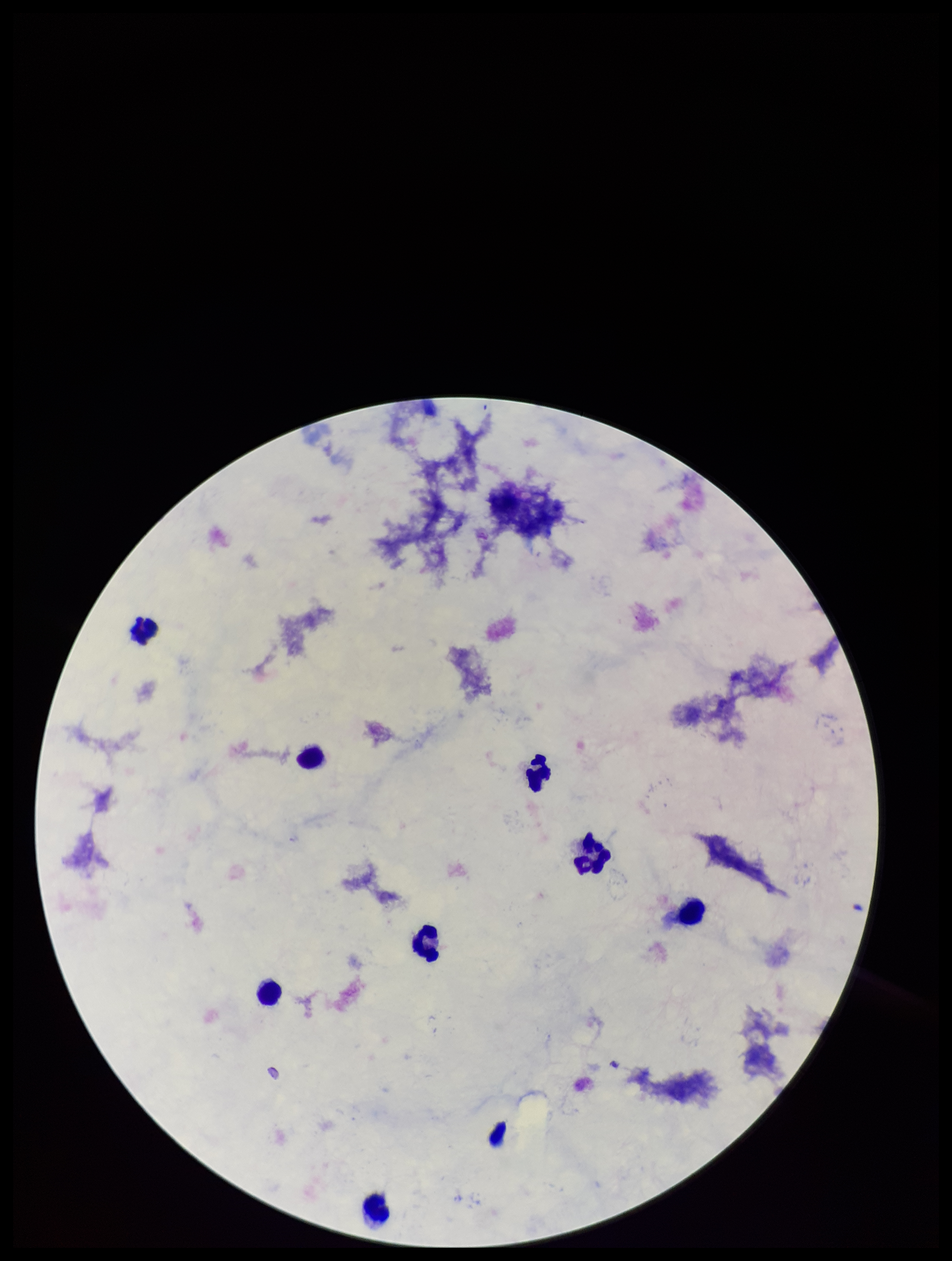

image_size: 952×1261 pixels
leukocyte_count: 8
capture: smartphone photograph through the microscope eyepiece
parasite_count: 0
patient_malaria_status: negative
plasmodium_parasites: none seen
preparation: thick smear
field_of_view: one from this slide
stain: Giemsa